Classify this cell by malaria status.
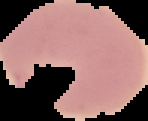
It is parasitized.

{
  "image_type": "cell region segmented out of the field of view; surrounding area masked to black",
  "preparation": "thin blood film",
  "image_size": "148×121 pixels"
}